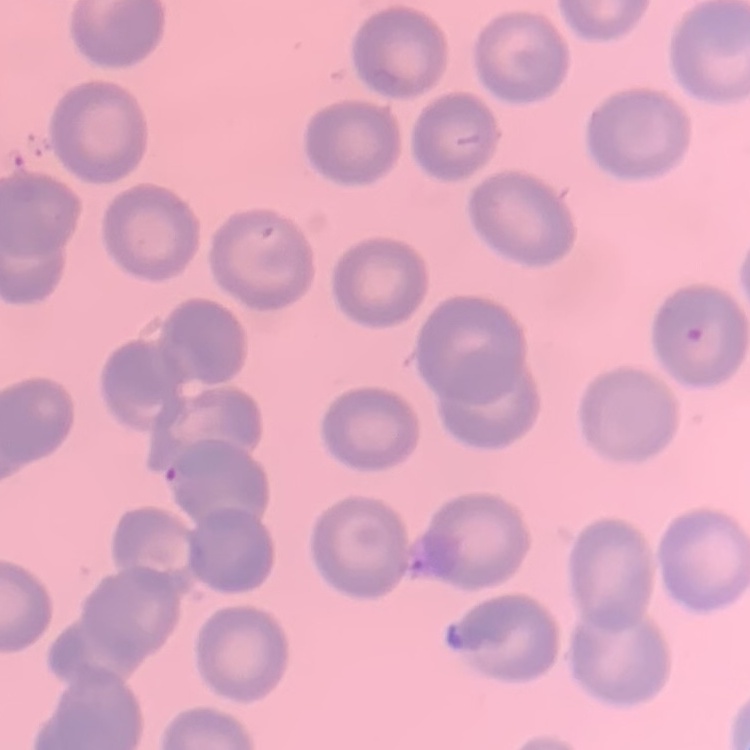

red blood cell morphology = no rouleaux formation
preparation = thin blood film
image type = one tile cut from a larger photomicrograph
stain = Field's or Giemsa